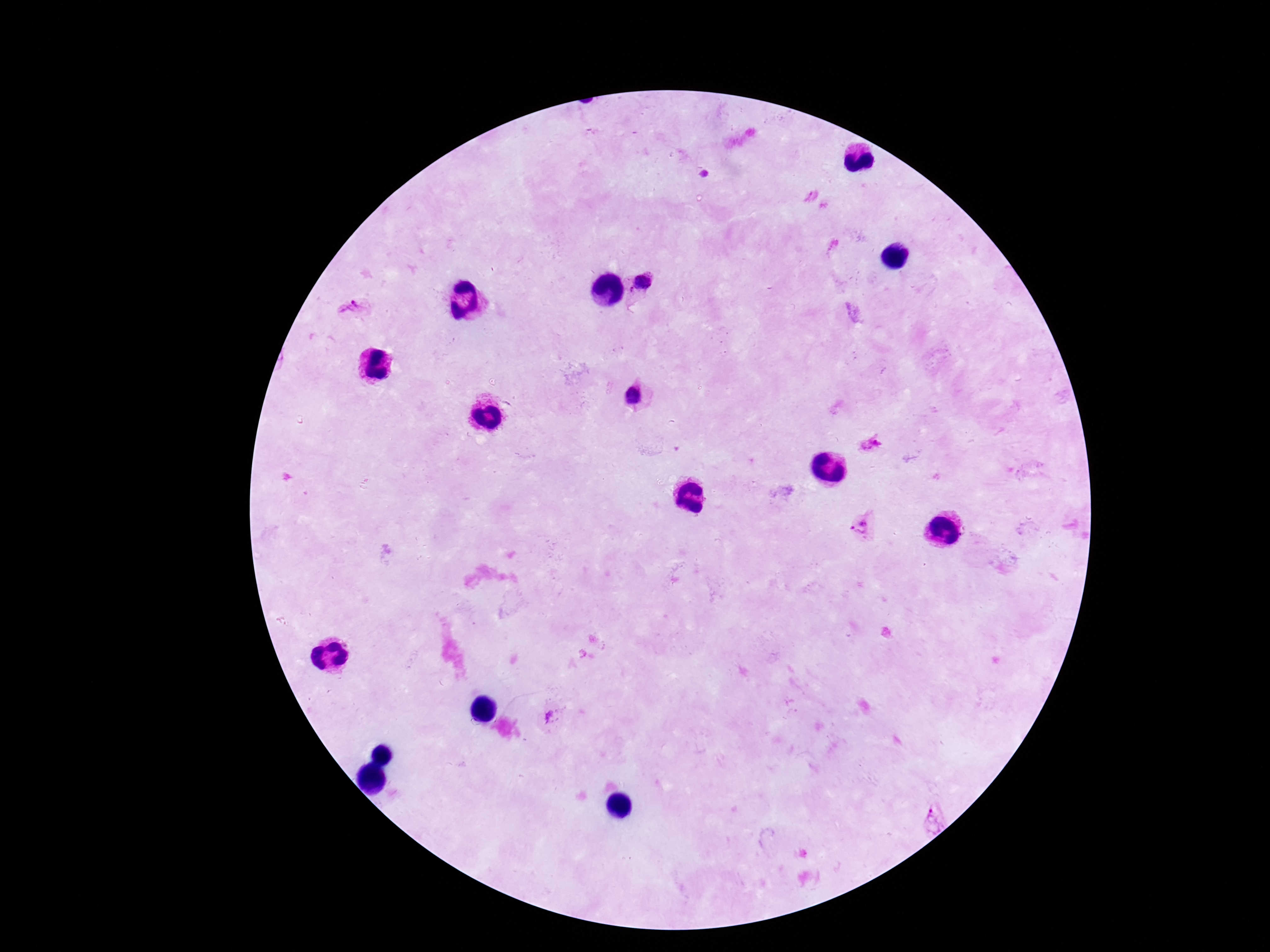
Approximate centers as (x, y) in pixels.
Summary:
  - Plasmodium parasite locations: (644, 284), (352, 307), (635, 397), (872, 444), (860, 526), (553, 716), (933, 819)
  - Preparation: thick peripheral-blood smear
  - Image size: 1270×952 pixels
  - Stain: Giemsa
  - Magnification: 100x
  - Patient malaria status: positive
  - Capture: smartphone camera through the microscope eyepiece
  - Field of view: one from this slide